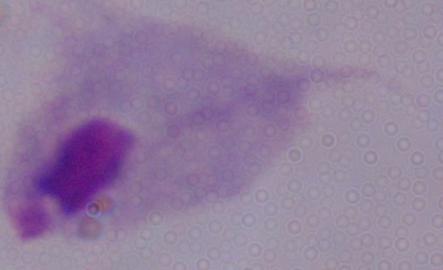
Summary:
  - Identification: trichomonad
  - Magnification: 1000x
  - Modality: micrograph